Classify this cell by malaria status.
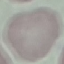

It is uninfected.

{
  "image_type": "automatically extracted cell patch, resized to 64 × 64 pixels",
  "stain": "Giemsa",
  "capture": "smartphone camera at the microscope eyepiece",
  "preparation": "thin smear"
}